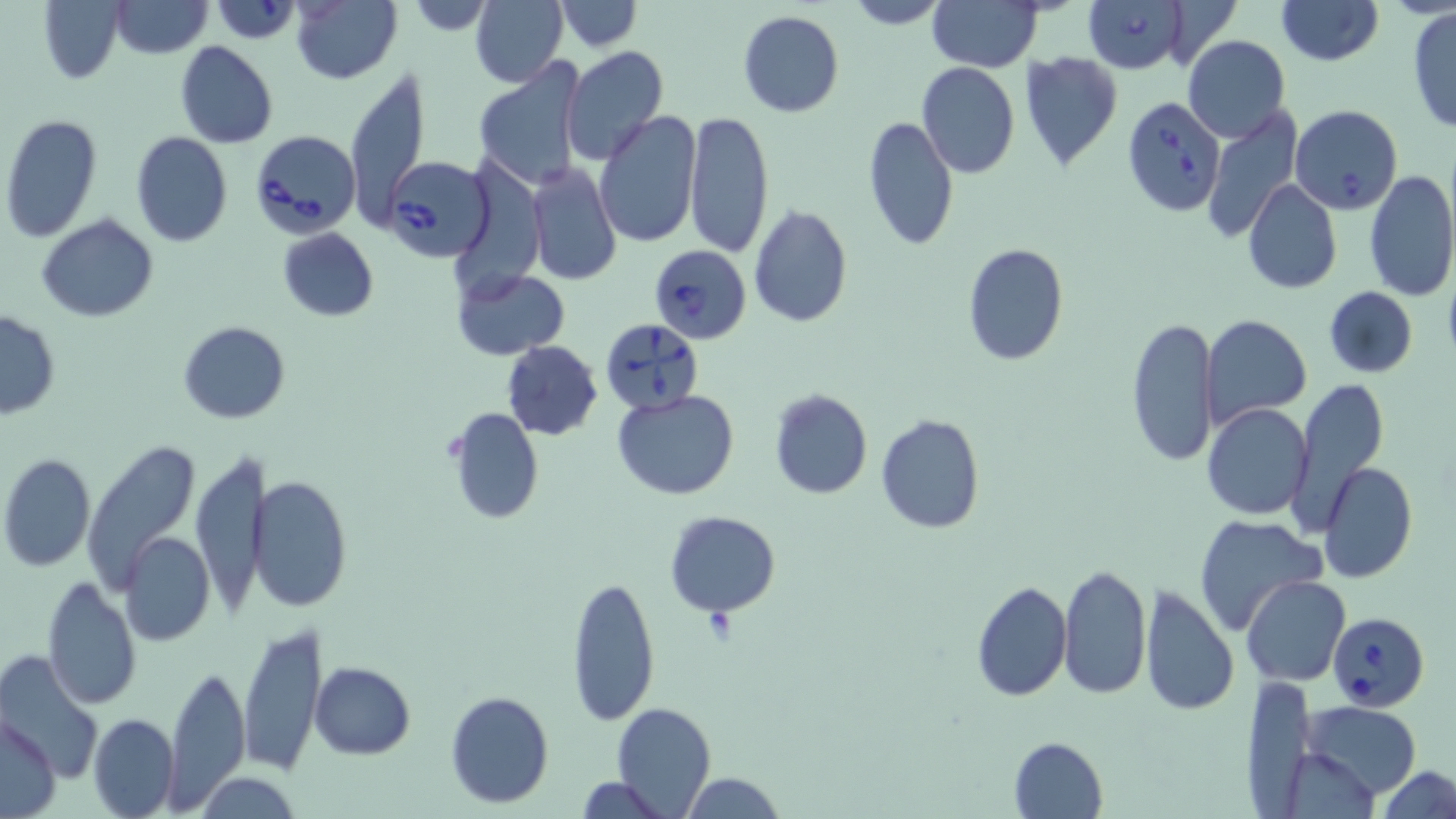
slide-level diagnosis = Babesia divergens
preparation = thin blood smear
modality = optical microscopy
Babesia divergens-infected red blood cell locations = approximate bounding boxes as (x1,y1)-(x2,y2) corner pairs in pixels: (1083,0)-(1188,74), (1122,94)-(1226,217), (250,130)-(359,238), (381,154)-(494,263), (649,245)-(751,344), (599,318)-(706,417), (1328,613)-(1429,710)
uninfected red blood cell locations = approximate bounding boxes as (x1,y1)-(x2,y2) corner pairs in pixels: (215,0)-(302,43), (407,0)-(498,36), (470,0)-(568,88), (554,0)-(641,50), (843,0)-(951,28), (927,0)-(1042,71), (1163,0)-(1241,71), (1276,0)-(1383,66), (39,1)-(125,83), (109,1)-(212,57), (290,1)-(403,84), (1408,8)-(1456,134), (737,9)-(844,117), (1183,35)-(1290,143), (176,42)-(278,149), (560,46)-(668,165), (1017,51)-(1124,171), (473,59)-(588,192), (916,62)-(1020,180), (343,64)-(430,229), (1201,104)-(1304,241), (1290,105)-(1402,214), (594,110)-(703,248), (685,110)-(774,256), (0,114)-(102,245), (863,114)-(959,254), (131,132)-(234,248), (526,163)-(621,285), (1362,169)-(1456,302), (1243,179)-(1342,293), (748,205)-(853,326), (37,215)-(158,323), (276,227)-(380,322), (962,243)-(1069,367), (452,267)-(569,361), (1323,285)-(1417,379), (0,311)-(61,419), (1200,315)-(1312,428), (1125,317)-(1220,469), (177,321)-(291,423), (501,340)-(603,441), (1286,377)-(1388,533), (768,389)-(874,499), (612,390)-(739,500), (1201,401)-(1315,522), (446,407)-(544,525), (876,413)-(987,533), (81,440)-(200,592), (190,451)-(264,612), (1,452)-(96,573), (1319,463)-(1419,584), (250,471)-(352,611), (663,510)-(780,616), (1193,516)-(1330,638), (118,531)-(215,646), (1058,563)-(1152,699), (565,574)-(661,728), (42,575)-(142,710), (1241,576)-(1350,687), (971,579)-(1072,702), (1138,584)-(1240,718), (239,621)-(324,776), (1,649)-(104,780), (310,662)-(415,758), (163,664)-(249,809), (1242,676)-(1318,813), (444,689)-(553,808), (1303,701)-(1423,800), (612,704)-(715,816), (88,713)-(179,818), (1,715)-(59,817), (1008,736)-(1108,819), (1278,746)-(1381,817), (1377,765)-(1456,819), (194,772)-(301,818), (681,772)-(786,818), (573,776)-(669,818)
platelet locations = approximate bounding boxes as (x1,y1)-(x2,y2) corner pairs in pixels: (703,605)-(738,643)
image size = 1456×819 pixels
stain = May-Grünwald-Giemsa
field of view = one of a larger specimen
magnification = 1000x